Outline each blood parasite and name the species.
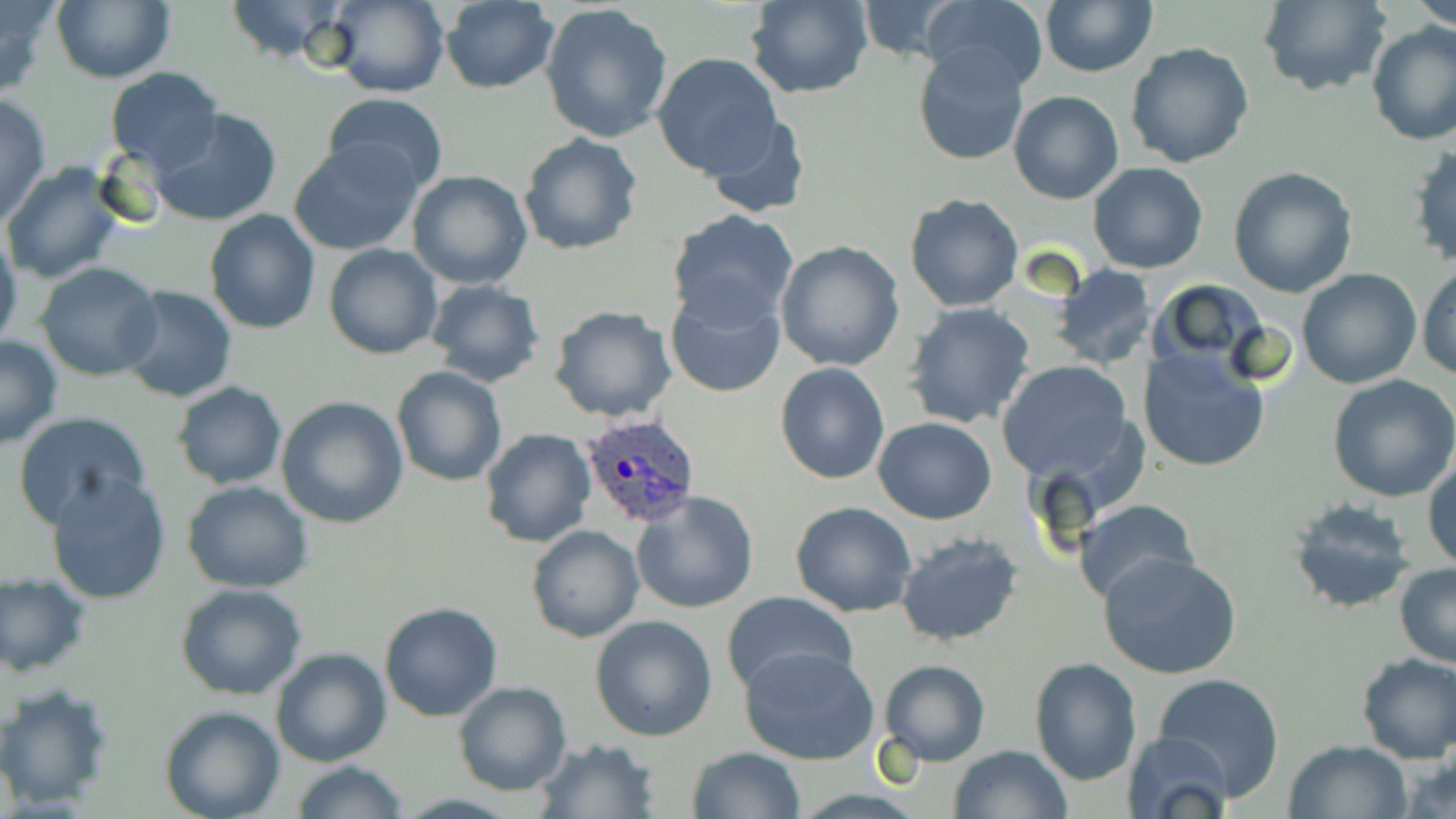
Approximate bounding boxes as named x1/y1/x2/y2 corners in pixels.
Plasmodium ovale-infected red blood cells: (x1=579, y1=412, x2=702, y2=529).
No Plasmodium falciparum, Plasmodium malariae, Plasmodium vivax, Babesia divergens, or Trypanosoma brucei observed.

Summary:
  - Uninfected red blood cell locations: (x1=0, y1=0, x2=57, y2=97), (x1=224, y1=0, x2=351, y2=64), (x1=327, y1=0, x2=450, y2=98), (x1=437, y1=0, x2=559, y2=93), (x1=852, y1=0, x2=971, y2=64), (x1=923, y1=0, x2=1049, y2=94), (x1=1257, y1=0, x2=1391, y2=95), (x1=1412, y1=0, x2=1456, y2=30), (x1=51, y1=1, x2=176, y2=83), (x1=746, y1=1, x2=875, y2=99), (x1=1041, y1=1, x2=1156, y2=76), (x1=540, y1=3, x2=674, y2=143), (x1=1366, y1=22, x2=1456, y2=148), (x1=1126, y1=42, x2=1255, y2=169), (x1=912, y1=45, x2=1032, y2=166), (x1=651, y1=52, x2=785, y2=179), (x1=105, y1=67, x2=225, y2=172), (x1=1009, y1=90, x2=1122, y2=203), (x1=0, y1=93, x2=51, y2=227), (x1=325, y1=93, x2=448, y2=195), (x1=149, y1=108, x2=282, y2=226), (x1=702, y1=115, x2=810, y2=219), (x1=518, y1=133, x2=644, y2=257), (x1=291, y1=139, x2=423, y2=257), (x1=1405, y1=142, x2=1456, y2=270), (x1=3, y1=162, x2=124, y2=284), (x1=1088, y1=163, x2=1210, y2=275), (x1=1228, y1=165, x2=1359, y2=298), (x1=406, y1=170, x2=532, y2=291), (x1=904, y1=194, x2=1026, y2=312), (x1=203, y1=209, x2=320, y2=334), (x1=668, y1=211, x2=801, y2=330), (x1=0, y1=232, x2=22, y2=355), (x1=775, y1=240, x2=906, y2=373), (x1=324, y1=244, x2=443, y2=360), (x1=36, y1=263, x2=164, y2=382), (x1=1416, y1=263, x2=1456, y2=380), (x1=1054, y1=266, x2=1156, y2=370), (x1=1296, y1=267, x2=1422, y2=389), (x1=1148, y1=277, x2=1277, y2=373), (x1=423, y1=280, x2=546, y2=387), (x1=118, y1=286, x2=237, y2=404), (x1=664, y1=288, x2=786, y2=399), (x1=903, y1=303, x2=1035, y2=428), (x1=548, y1=306, x2=677, y2=424), (x1=0, y1=335, x2=62, y2=449), (x1=1138, y1=346, x2=1271, y2=472), (x1=996, y1=360, x2=1137, y2=480), (x1=775, y1=362, x2=890, y2=484), (x1=391, y1=366, x2=506, y2=485), (x1=1326, y1=373, x2=1456, y2=502), (x1=172, y1=382, x2=286, y2=489), (x1=276, y1=396, x2=408, y2=527), (x1=11, y1=410, x2=150, y2=529), (x1=874, y1=417, x2=997, y2=524), (x1=479, y1=427, x2=596, y2=548), (x1=1424, y1=457, x2=1456, y2=572), (x1=46, y1=474, x2=172, y2=604), (x1=181, y1=481, x2=314, y2=591), (x1=631, y1=491, x2=760, y2=614), (x1=1074, y1=498, x2=1201, y2=607), (x1=1288, y1=498, x2=1417, y2=613), (x1=790, y1=501, x2=918, y2=618), (x1=526, y1=524, x2=644, y2=642), (x1=894, y1=533, x2=1024, y2=645), (x1=1099, y1=552, x2=1244, y2=681), (x1=1393, y1=563, x2=1456, y2=669), (x1=0, y1=572, x2=91, y2=676), (x1=175, y1=582, x2=308, y2=700), (x1=722, y1=593, x2=857, y2=699), (x1=379, y1=602, x2=503, y2=721), (x1=589, y1=614, x2=718, y2=740), (x1=739, y1=644, x2=882, y2=766), (x1=271, y1=647, x2=392, y2=767), (x1=1354, y1=652, x2=1456, y2=762), (x1=879, y1=658, x2=989, y2=766), (x1=1028, y1=658, x2=1143, y2=786), (x1=1153, y1=672, x2=1285, y2=800), (x1=452, y1=680, x2=572, y2=796), (x1=0, y1=681, x2=115, y2=810), (x1=160, y1=706, x2=285, y2=819), (x1=1122, y1=732, x2=1235, y2=819), (x1=536, y1=736, x2=659, y2=817), (x1=1282, y1=739, x2=1412, y2=819), (x1=950, y1=744, x2=1071, y2=819), (x1=1397, y1=744, x2=1456, y2=817), (x1=687, y1=747, x2=805, y2=819), (x1=289, y1=761, x2=410, y2=818)
  - Slide-level diagnosis: Plasmodium ovale
  - Magnification: 1000x
  - Image size: 1456×819 pixels
  - Stain: May-Grünwald-Giemsa
  - Preparation: thin blood smear
  - Modality: light microscopy
  - Field of view: single